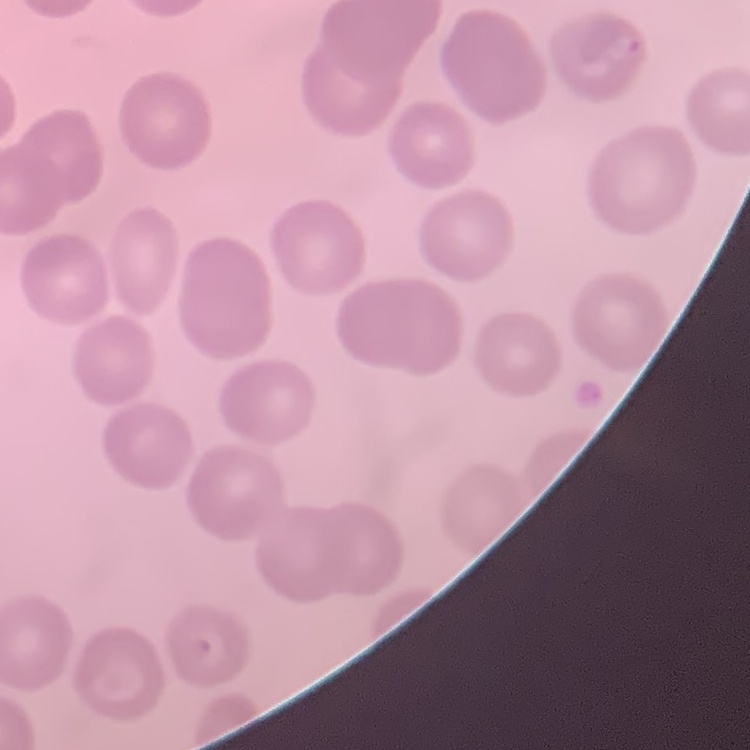
Summary:
  - Erythrocyte morphology: no rouleaux formation
  - Image type: square crop of a larger photomicrograph
  - Preparation: thin blood smear
  - Stain: Field's or Giemsa